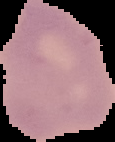
result = no malaria parasites detected
image size = 115×142 pixels
preparation = thin blood film
image type = segmented cell region on a black background